Identify the blood parasite species.
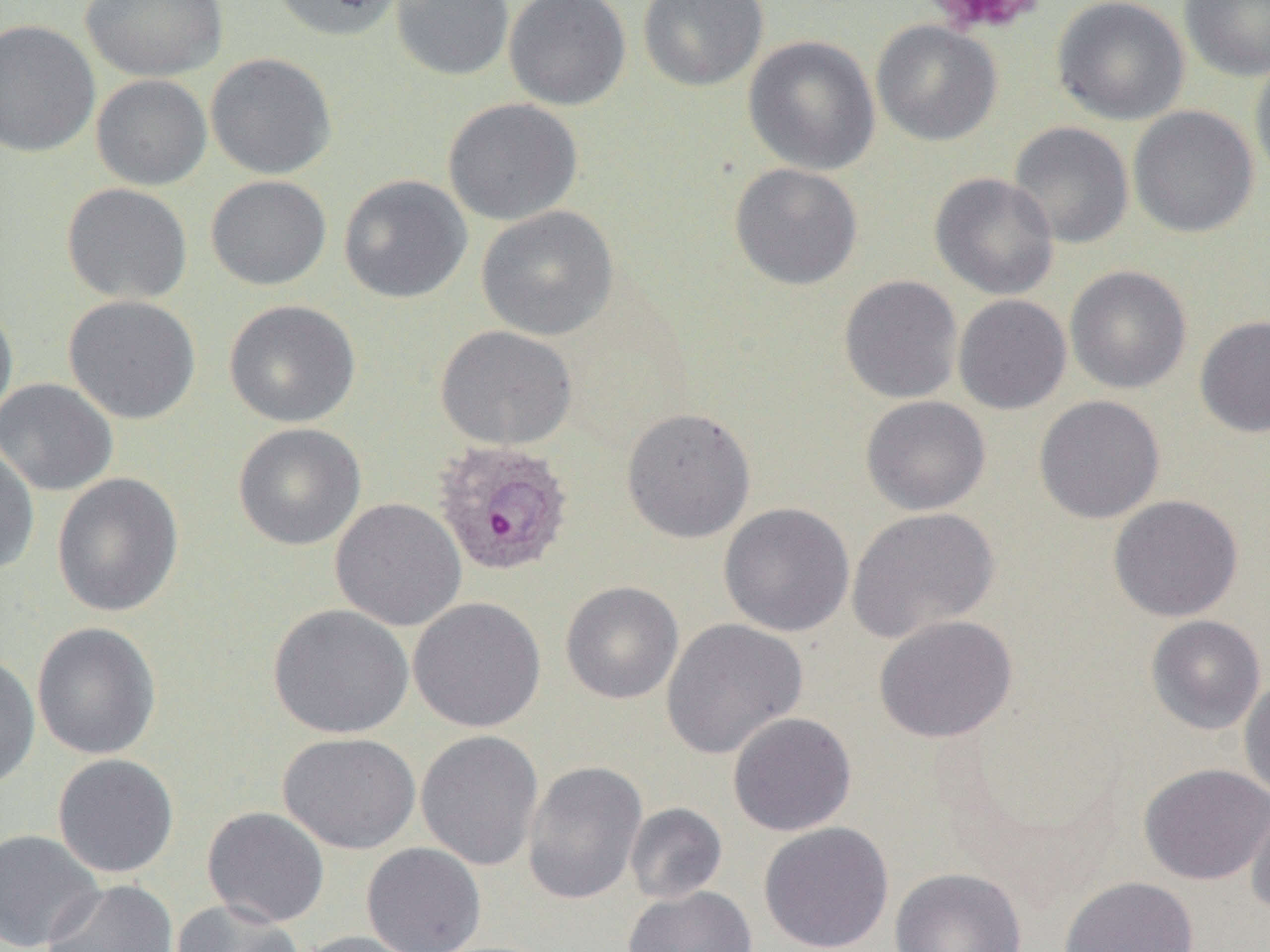
Plasmodium ovale.

{
  "modality": "light microscopy",
  "field_of_view": "one of a larger specimen",
  "magnification": "1000x",
  "image_size": "1270×952 pixels",
  "plasmodium_ovale_infected_red_blood_cell_locations": "approximate bounding boxes as (x1,y1)-(x2,y2) corner pairs in pixels: (432,439)-(575,578)",
  "platelet_locations": "approximate bounding boxes as (x1,y1)-(x2,y2) corner pairs in pixels: (921,0)-(1046,36)",
  "uninfected_red_blood_cell_locations": "approximate bounding boxes as (x1,y1)-(x2,y2) corner pairs in pixels: (81,0)-(229,82), (270,0)-(406,42), (390,0)-(514,81), (503,0)-(631,110), (637,0)-(769,91), (1051,0)-(1190,126), (1180,0)-(1270,81), (0,19)-(100,158), (871,20)-(1003,146), (743,35)-(881,176), (205,52)-(337,180), (1250,52)-(1270,189), (91,74)-(212,191), (442,98)-(583,225), (1128,105)-(1259,238), (1008,121)-(1134,249), (729,163)-(863,290), (929,172)-(1060,300), (338,174)-(472,304), (205,175)-(332,290), (61,182)-(192,305), (476,205)-(619,341), (1064,265)-(1192,395), (839,275)-(963,404), (63,294)-(200,425), (953,294)-(1072,414), (0,299)-(18,430), (223,299)-(360,427), (1195,315)-(1270,438), (435,325)-(578,450), (0,378)-(118,496), (860,395)-(991,516), (1033,395)-(1166,524), (621,407)-(756,543), (232,422)-(366,550), (0,443)-(40,576), (51,472)-(184,617), (1108,495)-(1243,622), (330,497)-(467,631), (718,502)-(855,637), (846,507)-(1000,644), (560,581)-(684,704), (408,596)-(546,733), (268,603)-(414,739), (873,614)-(1017,743), (1145,615)-(1266,734), (661,618)-(808,759), (31,622)-(162,760), (0,652)-(40,792), (1239,675)-(1270,802), (728,711)-(857,836), (415,729)-(544,871), (277,732)-(421,854), (52,753)-(180,878), (522,760)-(648,905), (1138,762)-(1270,885), (1246,792)-(1270,916), (625,802)-(728,904), (202,806)-(330,928), (758,821)-(894,952), (0,829)-(105,952), (361,842)-(487,952), (889,867)-(1027,952), (1059,875)-(1199,952), (42,879)-(179,952), (622,886)-(758,952), (170,900)-(303,952), (294,931)-(426,952)",
  "preparation": "thin blood smear"
}